Identify the parasite.
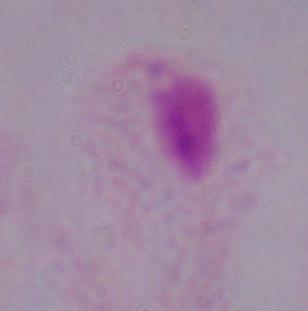

A trichomonad.

Summary:
  - Modality: photomicrograph
  - Magnification: 1000x